State the preparation type.
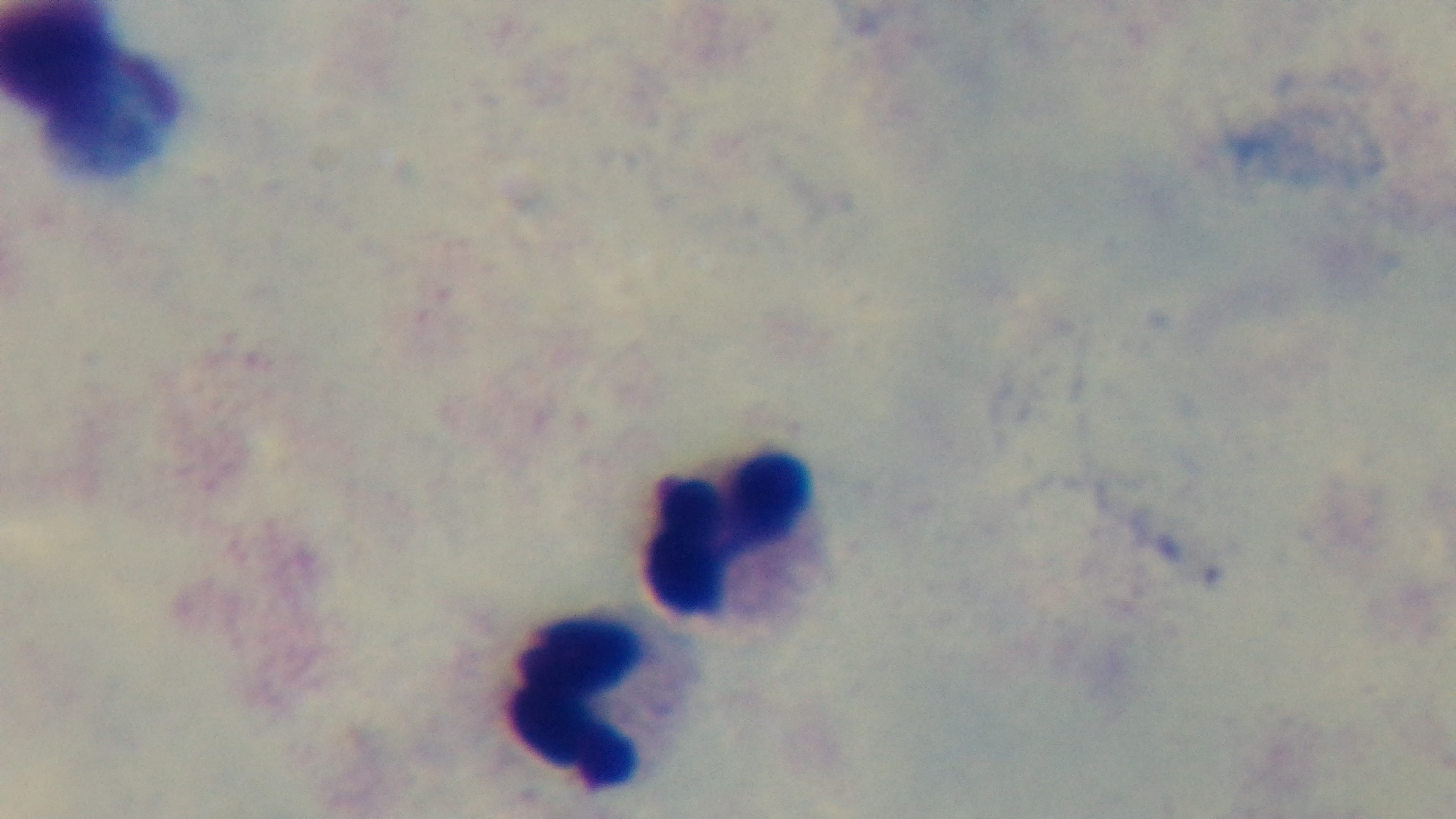
A thick smear.

objective = 100x oil immersion
stain = Giemsa
malaria status = uninfected
field of view = single
modality = light microscopy
capture = mounted 4K digital camera